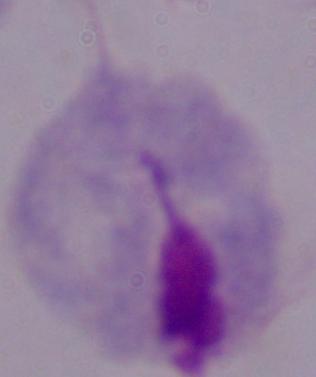

Micrograph. A trichomonad is seen. 1000x magnification.